Name the blood parasite species.
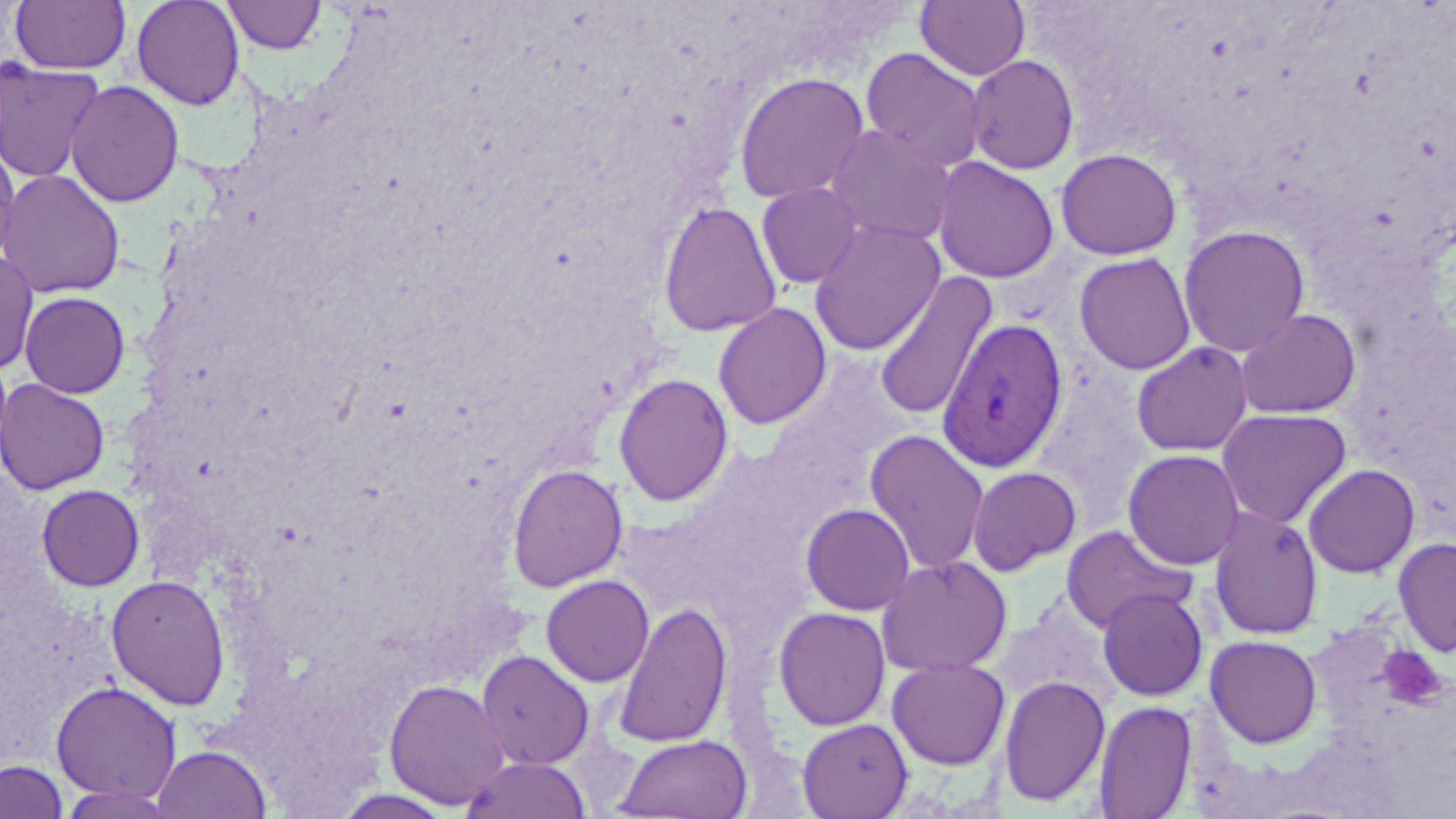

Plasmodium vivax.

{
  "modality": "light microscopy",
  "plasmodium_vivax_infected_red_blood_cell_locations": "approximate bounding boxes as (x1, y1, x2, y2) in pixels: (938, 317, 1068, 473)",
  "field_of_view": "single",
  "platelet_locations": "approximate bounding boxes as (x1, y1, x2, y2) in pixels: (1375, 641, 1444, 708)",
  "magnification": "1000x",
  "stain": "May-Grünwald-Giemsa",
  "image_size": "1456×819 pixels",
  "preparation": "thin blood smear",
  "uninfected_red_blood_cell_locations": "approximate bounding boxes as (x1, y1, x2, y2) in pixels: (130, 0, 246, 111), (221, 0, 328, 55), (10, 1, 131, 74), (916, 1, 1030, 81), (861, 47, 987, 172), (966, 54, 1080, 175), (0, 59, 106, 183), (733, 71, 871, 205), (65, 79, 185, 208), (824, 124, 957, 248), (0, 138, 21, 268), (1056, 148, 1182, 260), (932, 156, 1059, 284), (0, 168, 126, 299), (756, 182, 864, 289), (658, 199, 782, 337), (809, 219, 945, 356), (1178, 225, 1310, 357), (0, 250, 40, 376), (1074, 252, 1196, 375), (873, 271, 998, 421), (20, 291, 130, 398), (712, 303, 831, 430), (1234, 308, 1361, 419), (1131, 341, 1254, 456), (613, 373, 733, 507), (0, 378, 110, 495), (1216, 408, 1352, 529), (864, 429, 990, 575), (1123, 449, 1246, 570), (506, 463, 629, 592), (1303, 463, 1420, 578), (967, 466, 1082, 576), (36, 484, 145, 592), (800, 503, 915, 616), (1208, 506, 1324, 641), (1060, 525, 1195, 633), (1393, 536, 1456, 658), (876, 555, 1013, 677), (105, 574, 231, 710), (541, 575, 655, 686), (1097, 588, 1209, 702), (993, 600, 1117, 711), (612, 601, 733, 749), (773, 606, 891, 731), (1205, 634, 1323, 748), (476, 650, 594, 770), (887, 657, 1010, 770), (998, 675, 1111, 807), (384, 679, 510, 810), (50, 681, 182, 803), (1094, 701, 1197, 818), (797, 718, 913, 819), (615, 734, 753, 818), (151, 744, 272, 818), (459, 756, 592, 819), (0, 760, 69, 819), (53, 784, 181, 818)"
}